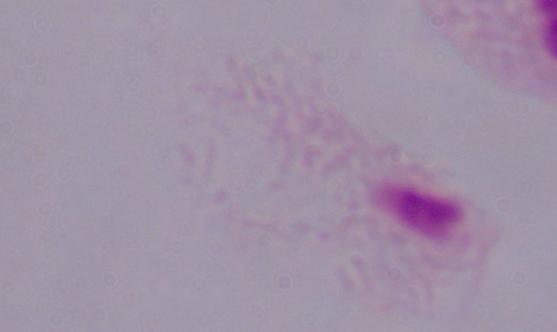
magnification = 1000x
identification = trichomonad
modality = micrograph